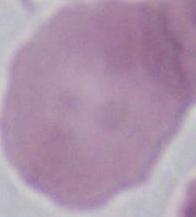

1000x magnification. Micrograph. An erythrocyte is shown.